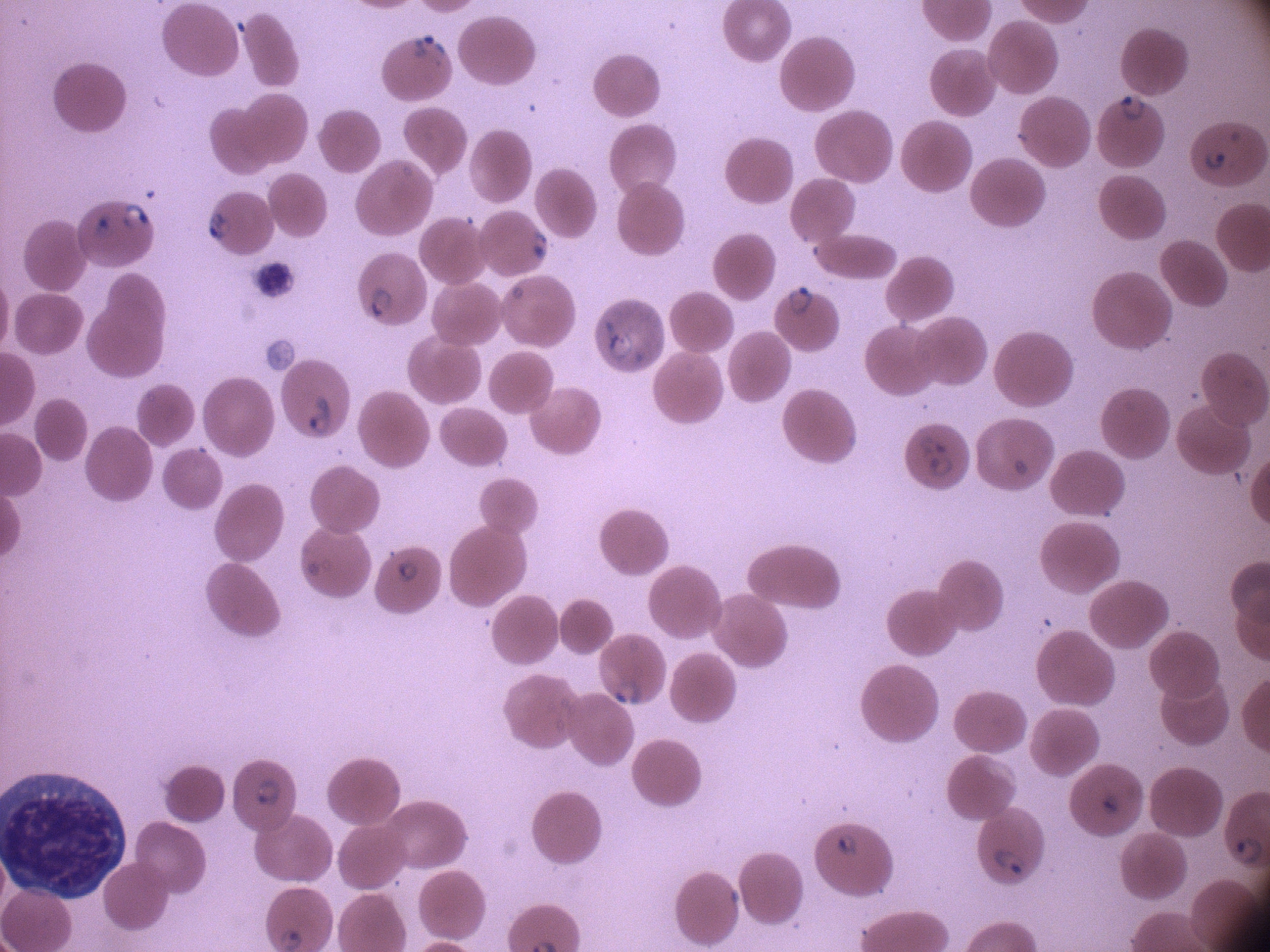 Approximate bounding boxes as (x1,y1)-(x2,y2) corner pairs in pixels, from the source annotation, which is not necessarily exhaustive. Ring form locations: (405,24)-(447,72), (1116,90)-(1151,126), (1199,142)-(1232,172), (115,195)-(157,238), (200,206)-(237,245), (84,209)-(117,243), (525,224)-(553,265), (785,278)-(817,319), (361,281)-(394,323), (599,313)-(638,367), (303,387)-(336,441), (914,429)-(950,457), (923,453)-(958,479), (391,552)-(420,585), (607,672)-(648,714), (249,775)-(288,811), (1082,787)-(1125,824), (831,828)-(863,862), (988,844)-(1031,881). Species: Plasmodium falciparum. Leica DM2000 optical microscope with a built-in camera. Captured at 100x magnification. Single field of view. Image is 1270×952 pixels. Giemsa stain. Thin blood smear.